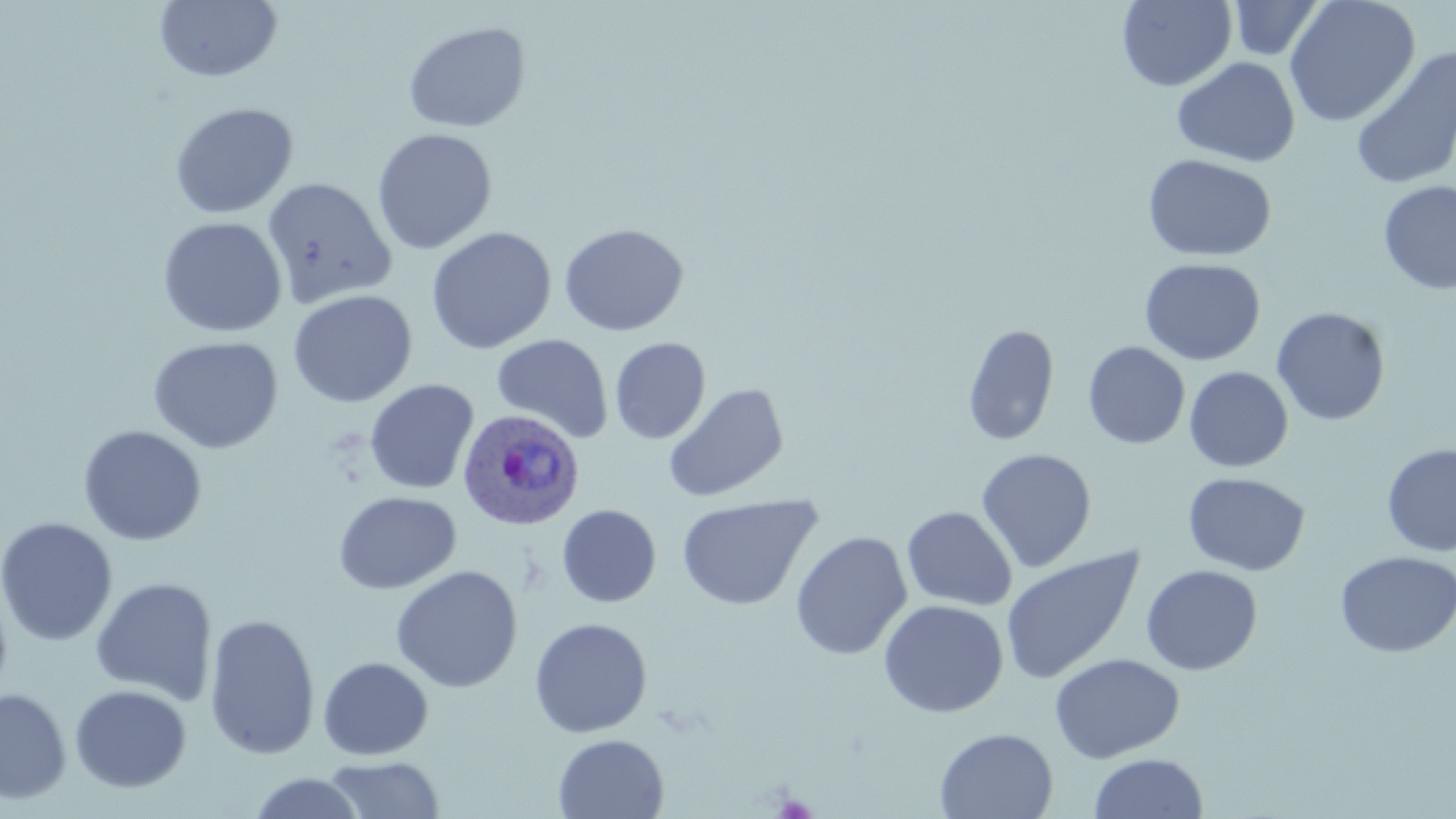

Summary:
  - Coordinate format: approximate bounding boxes as [x1, y1, x2, y2] in pixels
  - Plasmodium ovale-infected red blood cell locations: [456, 408, 585, 532]
  - Uninfected red blood cell locations: [155, 0, 282, 83], [1117, 0, 1237, 91], [1284, 0, 1420, 127], [1228, 1, 1325, 61], [403, 21, 531, 133], [1351, 47, 1456, 191], [1172, 56, 1301, 168], [169, 102, 299, 219], [372, 128, 497, 255], [1142, 153, 1276, 263], [262, 177, 397, 309], [1377, 180, 1456, 296], [158, 216, 287, 338], [559, 223, 689, 337], [426, 226, 557, 355], [1139, 257, 1265, 366], [287, 289, 418, 408], [1271, 306, 1391, 426], [961, 324, 1060, 448], [491, 334, 614, 443], [147, 335, 284, 453], [609, 337, 711, 444], [1083, 341, 1190, 450], [1184, 366, 1293, 472], [364, 379, 479, 495], [663, 382, 789, 502], [77, 424, 208, 546], [1382, 443, 1456, 557], [975, 447, 1097, 573], [1183, 471, 1310, 576], [333, 490, 461, 595], [675, 493, 823, 611], [556, 504, 662, 608], [901, 505, 1017, 611], [0, 516, 118, 645], [790, 530, 912, 660], [1000, 546, 1145, 685], [1335, 551, 1456, 658], [1141, 564, 1263, 675], [390, 565, 523, 694], [90, 577, 218, 706], [0, 587, 13, 705], [878, 599, 1009, 718], [203, 612, 320, 760], [529, 617, 653, 738], [1049, 652, 1185, 763], [317, 656, 434, 761], [70, 684, 192, 793], [0, 687, 71, 804], [934, 727, 1058, 818], [553, 733, 669, 819], [1088, 753, 1208, 819], [322, 755, 445, 818], [248, 772, 367, 818]
  - Slide-level diagnosis: Plasmodium ovale
  - Preparation: thin blood smear
  - Field of view: single
  - Modality: light microscopy
  - Stain: May-Grünwald-Giemsa
  - Magnification: 1000x
  - Image size: 1456×819 pixels